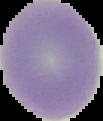

{
  "preparation": "thin blood smear",
  "image_size": "103×121 pixels",
  "malaria_status": "uninfected",
  "image_type": "segmented cell region on a black background"
}